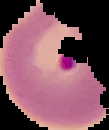
result: malaria parasites identified
image_type: segmented cell region with the area outside set to black
image_size: 109×130 pixels
preparation: thin blood film